Give the extent of all Plasmodium malariae-infected red blood cells.
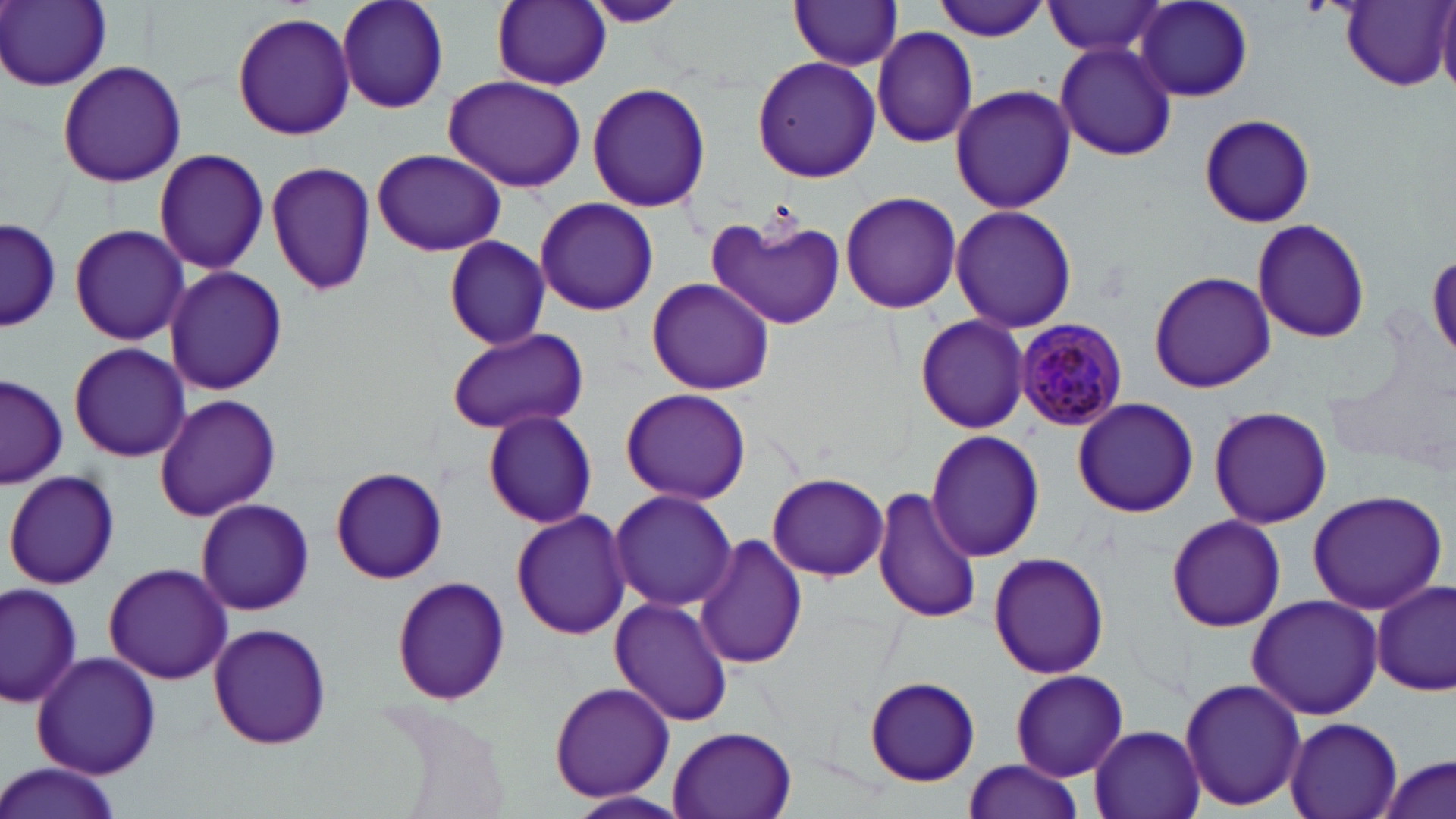
Approximate bounding boxes as (x1,y1)-(x2,y2) corner pairs in pixels.
Plasmodium malariae-infected red blood cells: (1013,320)-(1131,429).

{
  "slide_level_diagnosis": "Plasmodium malariae",
  "field_of_view": "one of a larger specimen",
  "magnification": "1000x",
  "image_size": "1456×819 pixels",
  "uninfected_red_blood_cell_locations": "approximate bounding boxes as (x1,y1)-(x2,y2) corner pairs in pixels: (2,0)-(112,91), (336,0)-(450,115), (489,0)-(614,91), (578,0)-(691,29), (930,0)-(1051,44), (788,1)-(904,71), (1043,1)-(1170,58), (1134,1)-(1255,102), (1339,1)-(1453,90), (1437,7)-(1456,98), (231,12)-(357,141), (871,26)-(978,148), (1054,40)-(1177,161), (752,56)-(880,182), (56,60)-(187,188), (443,72)-(588,193), (586,82)-(711,213), (949,84)-(1075,212), (1199,112)-(1316,228), (150,146)-(270,276), (371,149)-(506,258), (266,159)-(375,299), (840,191)-(962,314), (534,195)-(659,316), (951,204)-(1077,334), (703,209)-(845,332), (2,218)-(60,333), (1251,218)-(1371,343), (69,223)-(189,347), (442,238)-(552,346), (1429,254)-(1456,362), (163,267)-(289,396), (1148,270)-(1277,393), (646,279)-(774,395), (915,315)-(1029,433), (443,325)-(590,438), (67,341)-(190,463), (1,375)-(67,489), (620,388)-(751,505), (154,393)-(281,520), (1070,398)-(1198,518), (1208,405)-(1332,531), (483,409)-(598,528), (488,426)-(611,618), (926,431)-(1046,561), (330,467)-(445,585), (5,468)-(121,591), (768,472)-(887,581), (873,486)-(983,625), (609,489)-(736,612), (1306,490)-(1447,614), (193,498)-(316,616), (511,508)-(631,640), (1166,514)-(1286,632), (694,533)-(807,670), (988,551)-(1110,680), (104,561)-(231,684), (390,574)-(511,705), (1372,578)-(1454,698), (1,580)-(81,708), (1246,594)-(1384,720), (609,596)-(735,727), (208,623)-(332,751), (32,650)-(160,778), (1010,669)-(1127,780), (864,676)-(980,785), (1178,677)-(1307,813), (547,681)-(675,804), (1283,716)-(1403,819), (667,724)-(800,819), (1088,726)-(1205,819), (1375,753)-(1454,819), (962,760)-(1086,819), (0,763)-(123,819), (569,791)-(691,817)",
  "preparation": "thin blood smear",
  "stain": "May-Grünwald-Giemsa",
  "modality": "optical microscopy"
}